Name the parasite shown.
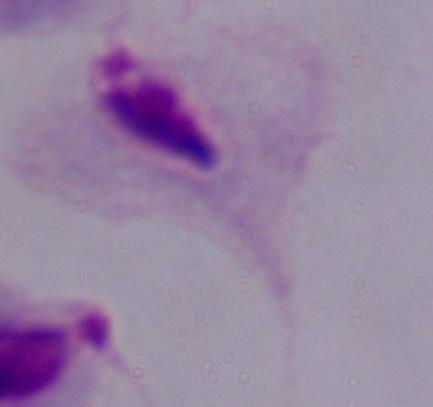

This is a trichomonad.

Summary:
  - Magnification: 1000x
  - Modality: photomicrograph